Identify the parasite.
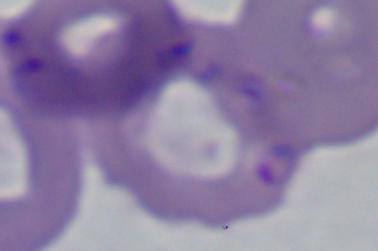
This is Babesia.

Photomicrograph. 1000x magnification.